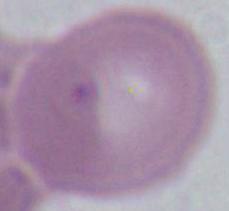

1000x magnification. An erythrocyte is seen. Micrograph.